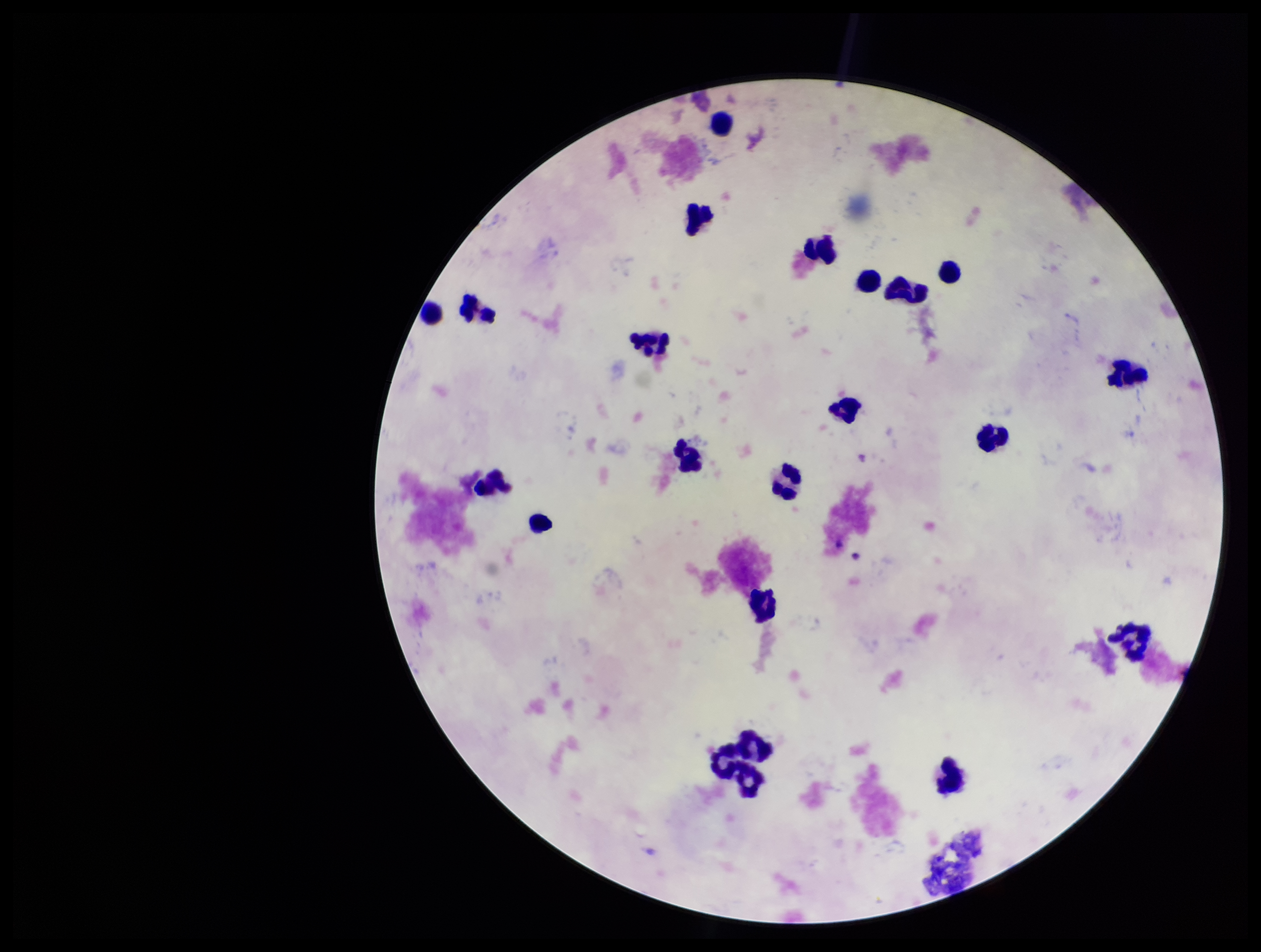 Leukocyte count: 21. Image is 1261×952 pixels. Plasmodium parasites: none detected. Photographed through the microscope eyepiece with a smartphone camera. Single field of view. Parasite count: 0. Stained with Giemsa. Preparation: thick. Patient malaria status: negative.